Assess this cell for malaria.
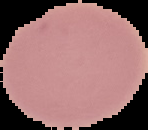

Uninfected.

image_size: 148×130 pixels
preparation: thin blood smear
image_type: cell region segmented out of the field of view; surrounding area masked to black